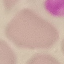 Result: negative for malaria parasites. Giemsa stain. Photographed with a smartphone camera at the microscope eyepiece. Cell patch, automatically extracted from a larger field of view and resized to 64 × 64 pixels. Thin blood smear.